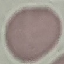
malaria_status: uninfected
preparation: thin blood smear
image_type: automatically extracted cell patch, resized to 64 × 64 pixels
stain: Giemsa
capture: smartphone camera at the microscope eyepiece